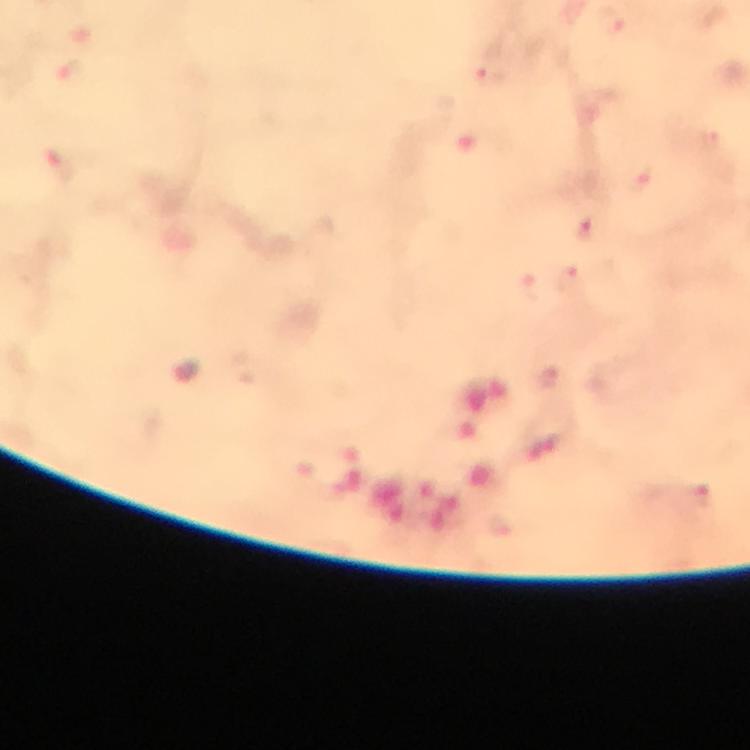
Approximate centers as {x, y} in pixels.
Summary:
  - Plasmodium parasite locations: {493, 77}, {585, 231}
  - Image size: 750×750 pixels
  - Magnification: 100x
  - Preparation: thick blood film
  - Immersion oil: used
  - Cropped from: one field of view
  - Context: from a diagnostic examination for malaria
  - Stain: Giemsa
  - Capture: smartphone photograph through a microscope